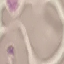

Summary:
  - Result: negative for malaria parasites
  - Image type: cell patch, automatically extracted from a larger field of view and resized to 64 × 64 pixels
  - Stain: Giemsa
  - Preparation: thin smear
  - Capture: smartphone camera at the microscope eyepiece